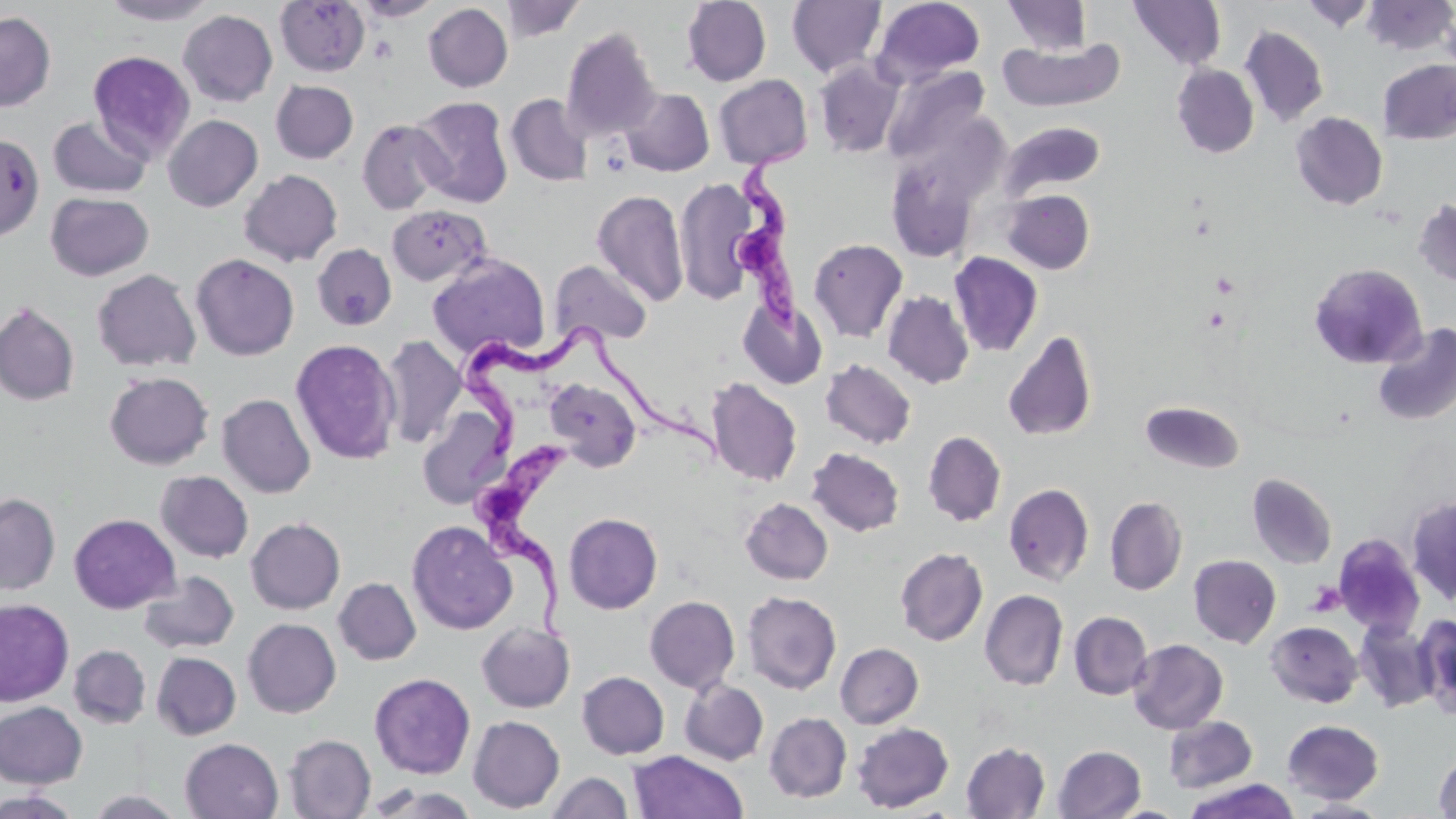
Summary:
  - Coordinate format: approximate bounding boxes as (x1,y1)-(x2,y2) corner pairs in pixels
  - Platelet locations: (1306,581)-(1346,617)
  - Uninfected red blood cell locations: (100,0)-(218,25), (499,0)-(587,41), (681,0)-(771,86), (871,0)-(986,87), (1002,0)-(1092,55), (1128,0)-(1226,71), (1362,0)-(1455,56), (275,1)-(369,77), (353,1)-(443,21), (786,1)-(887,78), (1301,1)-(1376,32), (423,3)-(513,92), (178,10)-(277,107), (0,11)-(56,111), (1239,26)-(1329,127), (560,27)-(661,142), (998,37)-(1124,112), (88,51)-(195,162), (1378,59)-(1456,145), (814,60)-(905,158), (1172,64)-(1259,158), (881,65)-(990,167), (713,74)-(813,169), (271,80)-(358,163), (620,88)-(714,176), (505,93)-(593,187), (410,97)-(513,208), (1291,112)-(1388,210), (163,115)-(263,212), (48,116)-(152,198), (357,119)-(450,215), (999,121)-(1105,200), (0,139)-(37,238), (886,157)-(982,263), (239,169)-(343,266), (674,178)-(763,305), (592,189)-(690,308), (1001,189)-(1095,274), (46,192)-(154,281), (1412,199)-(1456,287), (386,204)-(492,287), (808,238)-(908,342), (312,244)-(397,330), (948,251)-(1043,357), (190,253)-(299,361), (428,254)-(550,360), (549,260)-(653,348), (1308,263)-(1427,373), (91,268)-(201,372), (883,291)-(974,389), (739,297)-(828,390), (0,301)-(80,406), (1372,323)-(1456,426), (1002,330)-(1098,442), (380,335)-(466,450), (290,339)-(402,465), (820,359)-(917,449), (104,371)-(214,470), (545,378)-(641,472), (706,378)-(802,487), (217,394)-(316,498), (1140,400)-(1245,474), (416,404)-(511,508), (923,430)-(1006,526), (807,447)-(904,536), (156,471)-(253,563), (1246,473)-(1337,569), (1004,482)-(1094,586), (0,493)-(61,595), (1407,495)-(1456,604), (1104,496)-(1187,595), (741,498)-(833,585), (564,512)-(662,614), (68,513)-(180,614), (246,517)-(345,614), (407,520)-(517,635), (1333,534)-(1426,637), (895,547)-(988,646), (1188,554)-(1281,648), (138,571)-(239,653), (334,577)-(421,665), (980,589)-(1068,690), (742,590)-(841,694), (644,595)-(740,694), (0,598)-(74,706), (1069,611)-(1152,699), (1414,612)-(1456,715), (243,618)-(341,718), (1266,621)-(1362,707), (1354,621)-(1438,712), (476,622)-(575,712), (1128,639)-(1228,734), (835,643)-(923,728), (68,644)-(151,728), (151,652)-(241,740), (577,671)-(669,759), (369,672)-(475,778), (680,680)-(769,766), (0,701)-(87,788), (764,712)-(851,803), (468,715)-(565,813), (1164,716)-(1257,793), (1282,719)-(1383,803), (852,722)-(954,813), (284,734)-(376,819), (180,738)-(283,819), (962,742)-(1050,818), (1053,744)-(1145,819), (629,751)-(748,819), (1434,752)-(1456,818), (546,771)-(633,819), (1182,778)-(1301,818), (363,783)-(482,819), (84,789)-(188,818), (0,790)-(81,818), (1294,797)-(1390,818), (1107,804)-(1189,818)
  - Trypanosoma brucei locations: (733,132)-(804,342), (461,321)-(727,466), (467,440)-(575,648)
  - Slide-level diagnosis: Trypanosoma brucei
  - Modality: light microscopy
  - Stain: May-Grünwald-Giemsa
  - Preparation: thin blood smear
  - Image size: 1456×819 pixels
  - Magnification: 1000x
  - Field of view: single